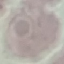 Result: no malaria parasites seen. Acquired by smartphone through the microscope eyepiece. Giemsa stain. Thin blood film. Cell patch, automatically extracted from a larger field of view and resized to 64 × 64 pixels.